Assess the morphology of the erythrocytes.
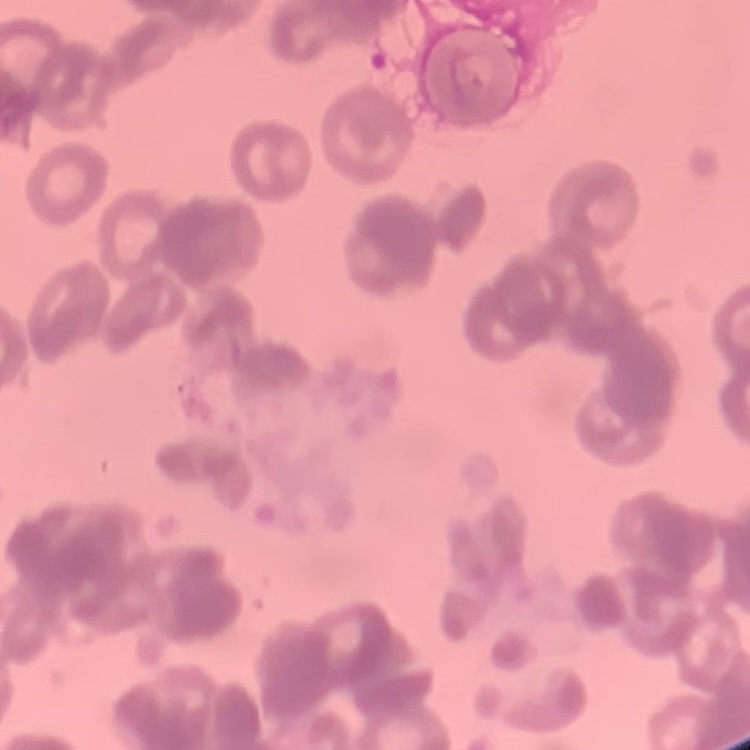
Rouleaux formation.

{
  "image_type": "one tile cut from a larger photomicrograph",
  "preparation": "thin blood film",
  "stain": "Field's or Giemsa"
}